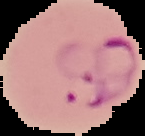

{
  "image_type": "cell region segmented out of the field of view; surrounding area masked to black",
  "result": "malaria parasites identified",
  "image_size": "145×136 pixels",
  "preparation": "thin blood film"
}